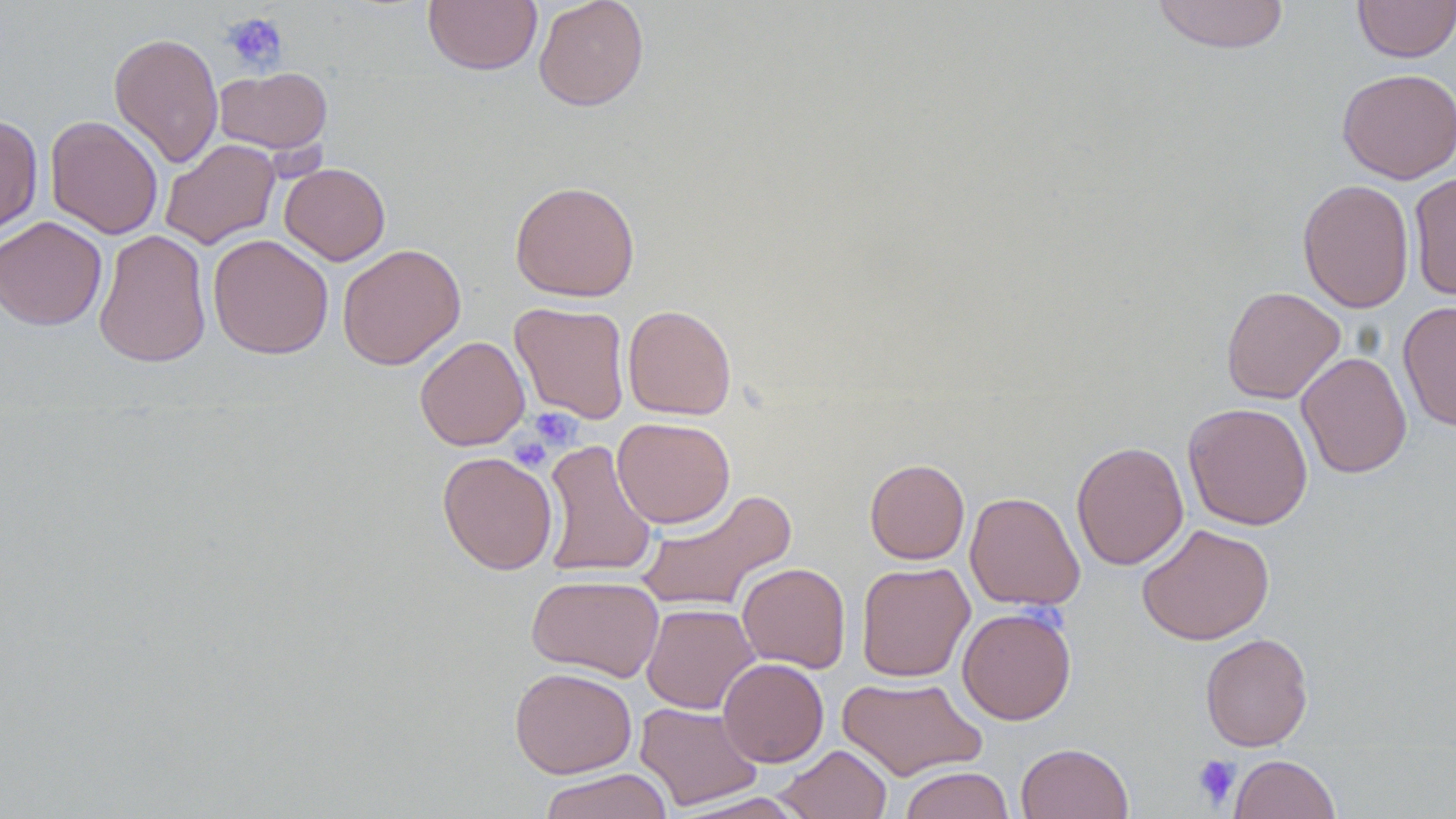 Approximate bounding boxes as named x1/y1/x2/y2 corners in pixels. Uninfected red blood cell locations: (x1=423, y1=0, x2=542, y2=75), (x1=533, y1=0, x2=649, y2=111), (x1=1151, y1=0, x2=1290, y2=54), (x1=1353, y1=1, x2=1455, y2=62), (x1=109, y1=32, x2=224, y2=169), (x1=215, y1=66, x2=332, y2=156), (x1=1336, y1=68, x2=1456, y2=184), (x1=0, y1=114, x2=43, y2=236), (x1=45, y1=115, x2=163, y2=239), (x1=160, y1=139, x2=281, y2=250), (x1=279, y1=162, x2=390, y2=265), (x1=1408, y1=170, x2=1456, y2=302), (x1=1297, y1=178, x2=1415, y2=313), (x1=509, y1=180, x2=641, y2=302), (x1=0, y1=216, x2=107, y2=331), (x1=93, y1=229, x2=212, y2=368), (x1=207, y1=234, x2=334, y2=359), (x1=337, y1=243, x2=466, y2=370), (x1=1221, y1=286, x2=1345, y2=404), (x1=1398, y1=300, x2=1456, y2=431), (x1=509, y1=301, x2=631, y2=424), (x1=622, y1=304, x2=737, y2=420), (x1=414, y1=335, x2=530, y2=450), (x1=1296, y1=351, x2=1412, y2=479), (x1=1183, y1=402, x2=1313, y2=530), (x1=612, y1=417, x2=735, y2=528), (x1=541, y1=438, x2=657, y2=580), (x1=1071, y1=441, x2=1189, y2=570), (x1=438, y1=451, x2=558, y2=575), (x1=865, y1=458, x2=969, y2=564), (x1=634, y1=489, x2=797, y2=614), (x1=965, y1=491, x2=1085, y2=611), (x1=1137, y1=523, x2=1274, y2=645), (x1=856, y1=561, x2=975, y2=682), (x1=737, y1=562, x2=851, y2=673), (x1=526, y1=574, x2=665, y2=682), (x1=641, y1=603, x2=759, y2=714), (x1=957, y1=606, x2=1076, y2=725), (x1=1200, y1=632, x2=1313, y2=752), (x1=717, y1=658, x2=829, y2=767), (x1=509, y1=666, x2=637, y2=778), (x1=837, y1=675, x2=987, y2=781), (x1=635, y1=702, x2=763, y2=810), (x1=1016, y1=742, x2=1134, y2=819), (x1=776, y1=744, x2=891, y2=819), (x1=1230, y1=754, x2=1341, y2=818), (x1=899, y1=766, x2=1015, y2=819), (x1=538, y1=768, x2=672, y2=819), (x1=671, y1=792, x2=813, y2=818). Platelet locations: (x1=220, y1=12, x2=288, y2=74), (x1=527, y1=408, x2=582, y2=451), (x1=509, y1=435, x2=552, y2=471), (x1=1193, y1=755, x2=1240, y2=809). Slide-level diagnosis: negative for blood parasites. Single field of view. Thin blood smear. 1000x magnification. May-Grünwald-Giemsa stain. Image is 1456×819 pixels. Light microscopy.